Identify the parasite.
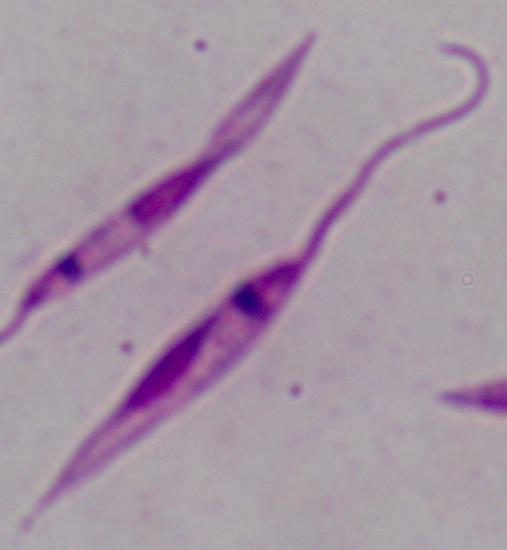

Leishmania.

modality = photomicrograph
magnification = 1000x